Locate every malaria parasite.
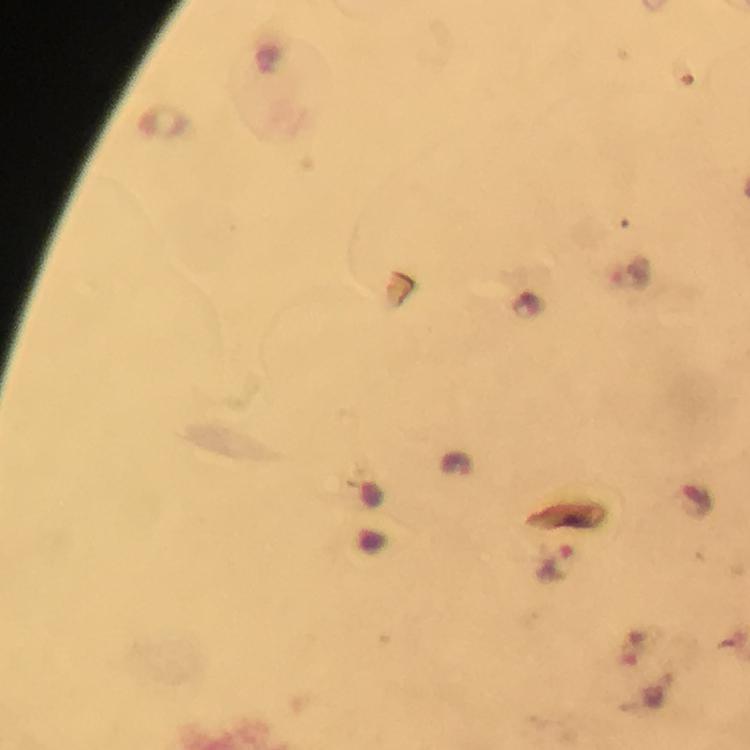

Approximate centers as (x, y) in pixels.
Malaria parasites: (558, 564).

immersion oil = applied
cropped from = a single field of view
image size = 750×750 pixels
stain = Giemsa
magnification = 100x
capture = smartphone camera through the microscope
context = from a malaria diagnostic workup
preparation = thick smear